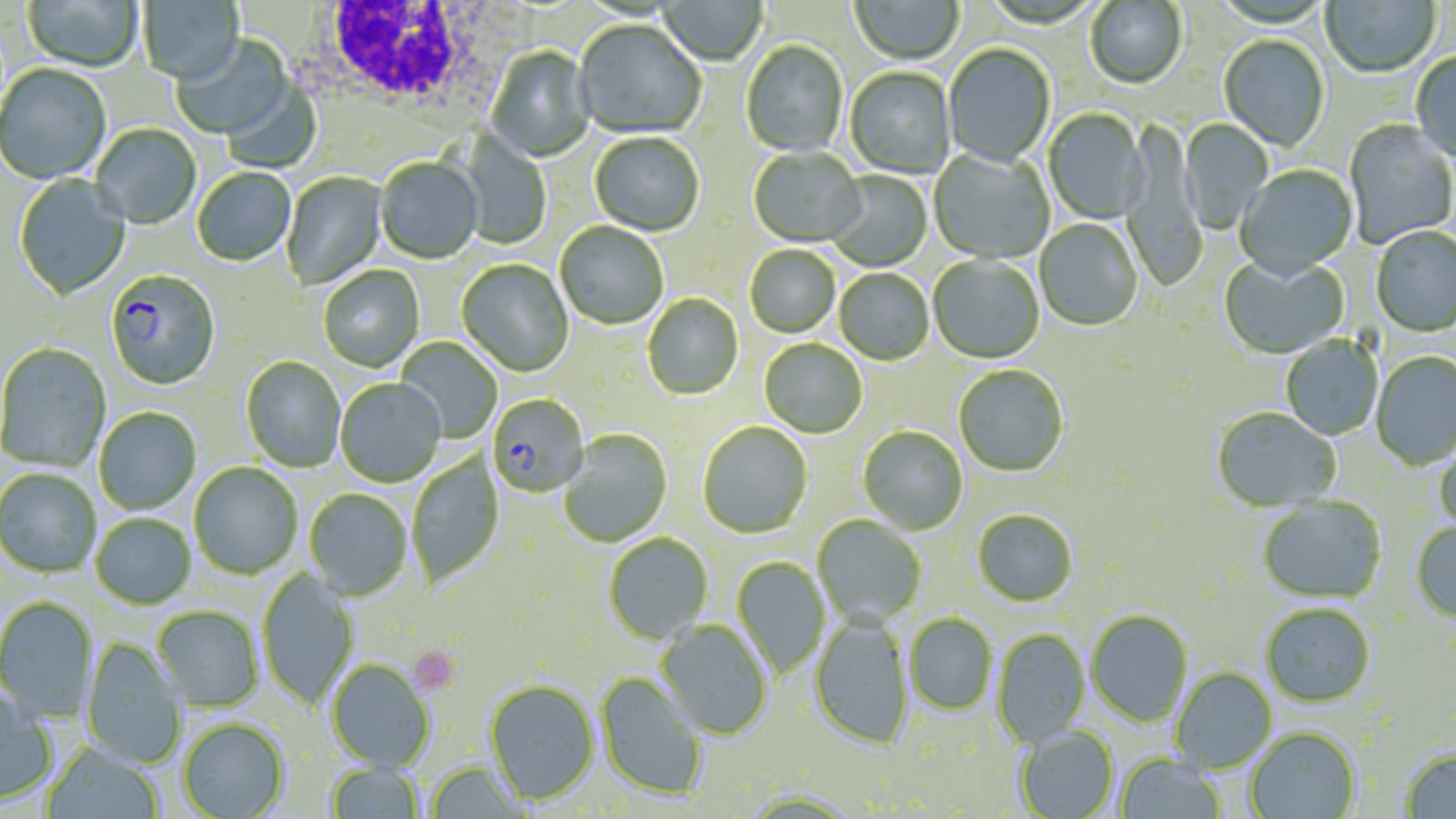
Summary:
  - Coordinate format: approximate bounding boxes as (x1,y1)-(x2,y2) corner pairs in pixels
  - Plasmodium falciparum-infected red blood cell locations: (106,270)-(221,392), (487,394)-(589,497)
  - Platelet locations: (409,646)-(460,695)
  - Uninfected red blood cell locations: (23,0)-(143,74), (138,0)-(245,86), (656,0)-(768,67), (850,0)-(964,66), (1322,0)-(1440,79), (1085,1)-(1187,91), (574,21)-(706,140), (171,34)-(294,141), (1218,36)-(1330,153), (741,41)-(848,158), (943,44)-(1056,169), (486,47)-(596,164), (1410,52)-(1456,167), (1,65)-(111,186), (845,68)-(955,180), (221,78)-(323,173), (1043,109)-(1148,226), (1179,119)-(1274,234), (1342,120)-(1456,249), (1121,123)-(1205,294), (91,124)-(202,231), (458,129)-(552,249), (590,133)-(704,237), (748,148)-(865,249), (928,148)-(1054,264), (375,158)-(484,264), (1235,165)-(1359,281), (192,168)-(296,268), (824,171)-(933,272), (281,172)-(387,290), (14,174)-(132,301), (1034,220)-(1143,331), (555,222)-(669,329), (1371,226)-(1456,337), (744,246)-(840,339), (1219,254)-(1350,360), (928,255)-(1044,364), (456,260)-(574,377), (318,265)-(425,373), (834,269)-(934,366), (643,294)-(743,400), (1281,335)-(1383,440), (396,337)-(503,444), (759,339)-(867,439), (0,344)-(111,473), (1371,352)-(1456,471), (241,357)-(346,473), (954,365)-(1069,477), (335,379)-(446,487), (94,407)-(201,515), (1212,407)-(1341,513), (697,421)-(813,538), (858,426)-(968,535), (559,429)-(673,548), (1433,439)-(1456,536), (406,453)-(504,588), (189,462)-(302,579), (0,468)-(101,578), (304,489)-(413,600), (1257,497)-(1387,604), (972,509)-(1079,607), (91,513)-(195,609), (812,515)-(926,628), (1410,521)-(1456,623), (603,533)-(713,645), (732,556)-(829,679), (258,569)-(360,709), (0,596)-(98,723), (1260,603)-(1376,707), (152,605)-(264,711), (1086,610)-(1193,727), (903,613)-(998,715), (809,615)-(913,750), (656,620)-(773,740), (992,628)-(1091,748), (80,638)-(187,769), (327,659)-(435,771), (1171,667)-(1277,773), (595,671)-(708,800), (485,680)-(600,804), (0,684)-(57,806), (178,718)-(289,819), (1014,725)-(1120,819), (1245,727)-(1361,819), (42,740)-(164,819), (1399,746)-(1456,818), (1115,754)-(1227,819), (324,762)-(425,819), (425,762)-(529,818)
  - White blood cell locations: (302,2)-(516,134)
  - Slide-level diagnosis: Plasmodium falciparum
  - Modality: light microscopy
  - Preparation: thin blood film
  - Magnification: 1000x
  - Image size: 1456×819 pixels
  - Field of view: one of a larger specimen
  - Stain: May-Grünwald-Giemsa